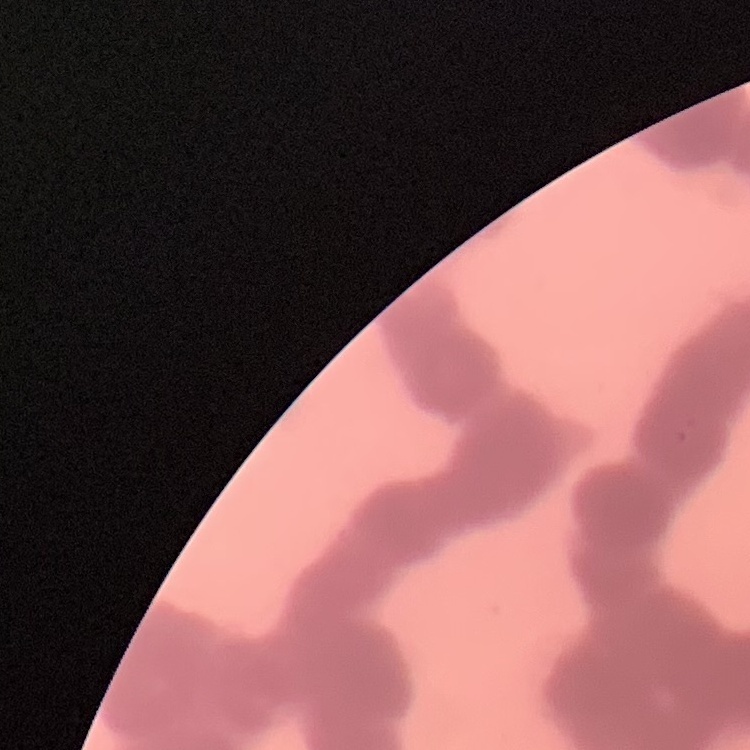

erythrocyte morphology = rouleaux formation
preparation = thin blood film
image type = one tile cut from a larger photomicrograph
stain = Field's or Giemsa